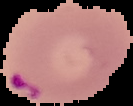 Image is 133×106 pixels. The area outside the segmented cell region is set to black. Result: Plasmodium parasites detected. From a thin blood film.